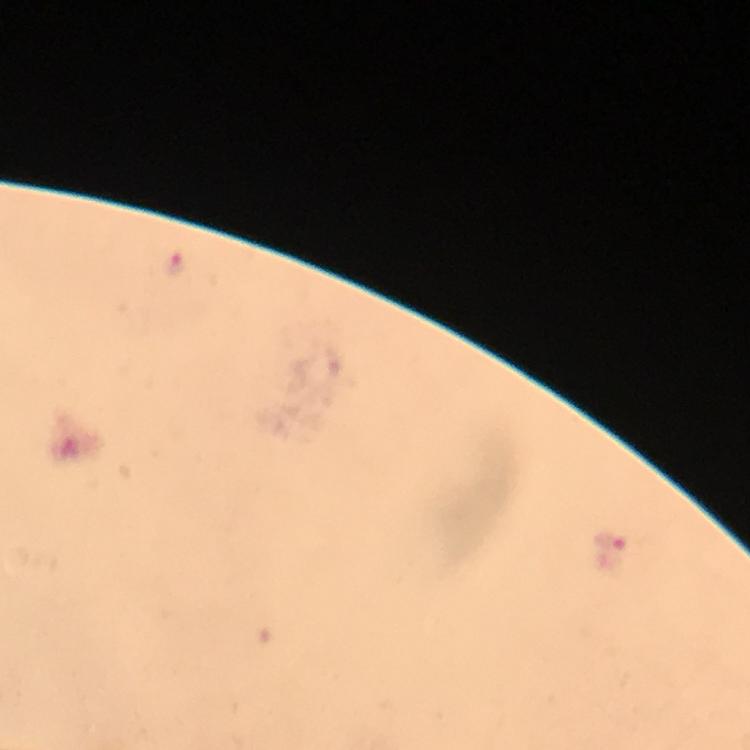
Approximate centers as {x, y} in pixels. Malaria parasite locations: {176, 265}, {610, 542}. Image is 750×750 pixels. A crop from one field of view. 100x magnification. Photographed through the microscope with a smartphone camera. From a diagnostic examination for malaria. Giemsa stain. Immersion oil was used. Thick blood film.